Report the malaria status of this cell.
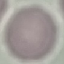
Uninfected.

Giemsa stain. Cell patch, automatically extracted from a larger field of view and resized to 64 × 64 pixels. Thin smear of blood. Photographed with a smartphone camera at the microscope eyepiece.